Classify this cell by malaria status.
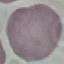

Uninfected.

Summary:
  - Stain: Giemsa
  - Image type: automatically extracted cell patch, resized to 64 × 64 pixels
  - Preparation: thin blood film
  - Capture: smartphone through the microscope eyepiece